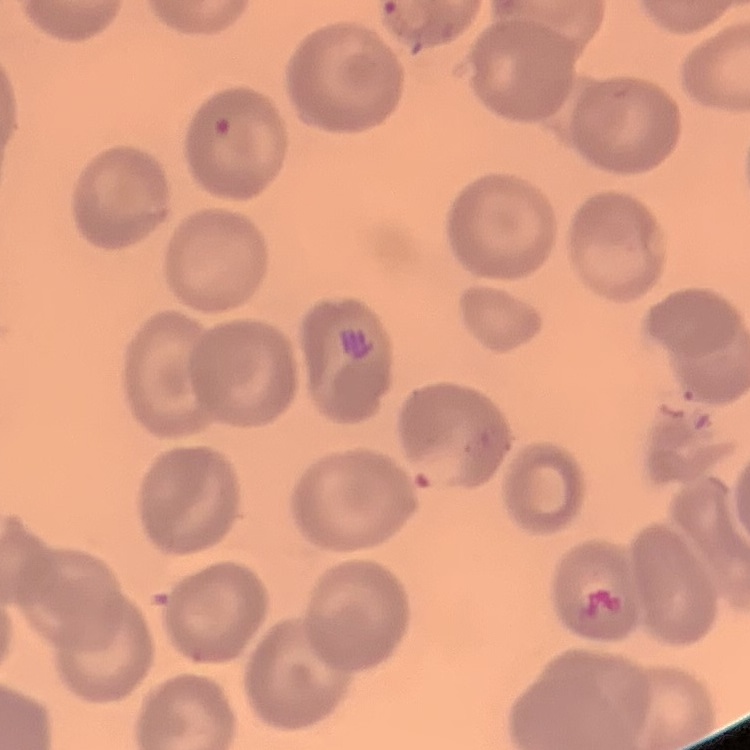
Summary:
  - Red blood cell morphology: no rouleaux formation
  - Stain: Field's or Giemsa
  - Preparation: thin peripheral smear
  - Image type: one tile cut from a larger photomicrograph